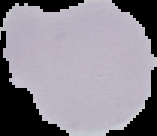

Summary:
  - Image size: 157×136 pixels
  - Image type: segmented cell region on a black background
  - Preparation: thin blood smear
  - Result: negative for malaria parasites